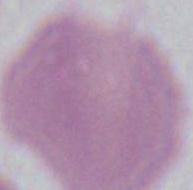 1000x magnification. An erythrocyte is seen. Micrograph.